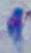
Summary:
  - Magnification: 1000x
  - Identification: Toxoplasma gondii
  - Modality: micrograph